Assess this cell for malaria.
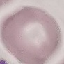
Uninfected.

Giemsa stain. Photographed with a smartphone camera at the microscope eyepiece. Thin blood smear. Cell patch, automatically extracted from a larger field of view and resized to 64 × 64 pixels.